Give the extent of all Plasmodium parasites.
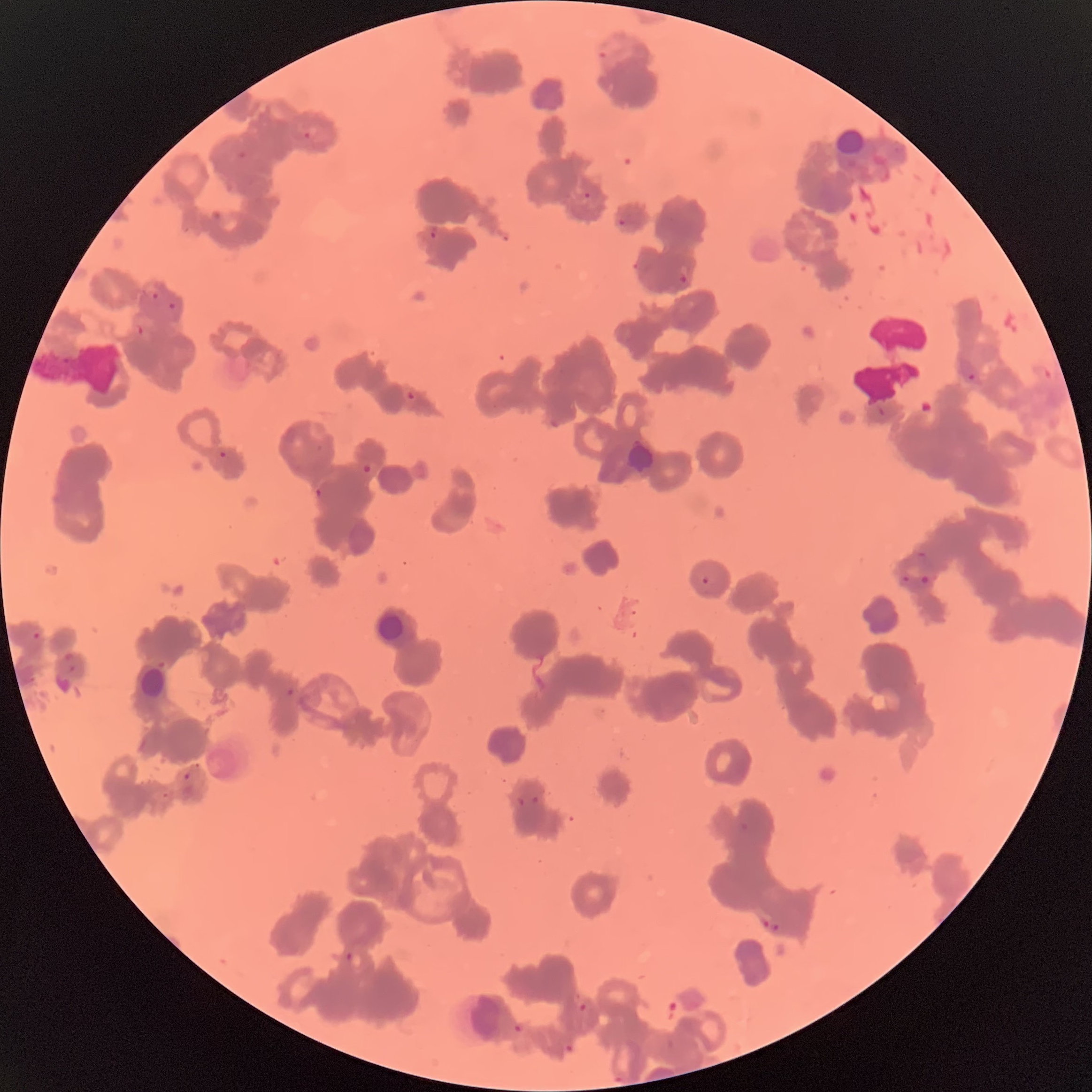

Approximate bounding boxes as (x1, y1, x2, y2) in pixels.
Plasmodium parasites: (596, 49, 613, 61), (301, 129, 315, 141), (236, 148, 250, 162), (583, 191, 592, 200), (617, 217, 627, 228), (429, 225, 439, 240), (632, 261, 643, 273), (678, 272, 688, 285), (150, 291, 161, 301), (167, 301, 178, 312), (136, 323, 146, 336), (959, 357, 979, 384), (402, 389, 419, 402), (877, 407, 888, 416), (218, 450, 228, 458), (361, 463, 376, 475), (313, 487, 323, 497), (915, 551, 930, 561), (901, 574, 910, 586), (918, 574, 932, 586), (700, 576, 710, 586), (31, 630, 41, 640), (65, 653, 76, 672), (285, 688, 295, 697), (182, 772, 191, 782), (161, 791, 171, 800), (530, 794, 541, 805), (517, 796, 526, 806), (739, 822, 751, 831), (761, 919, 770, 929), (771, 920, 783, 934), (344, 951, 355, 962), (577, 1001, 588, 1013), (512, 1024, 523, 1035), (562, 1041, 576, 1054), (611, 1069, 626, 1084).

The red blood cells show rouleaux formation. Optical microscopy. Image is 1092×1092 pixels. Thin blood smear.